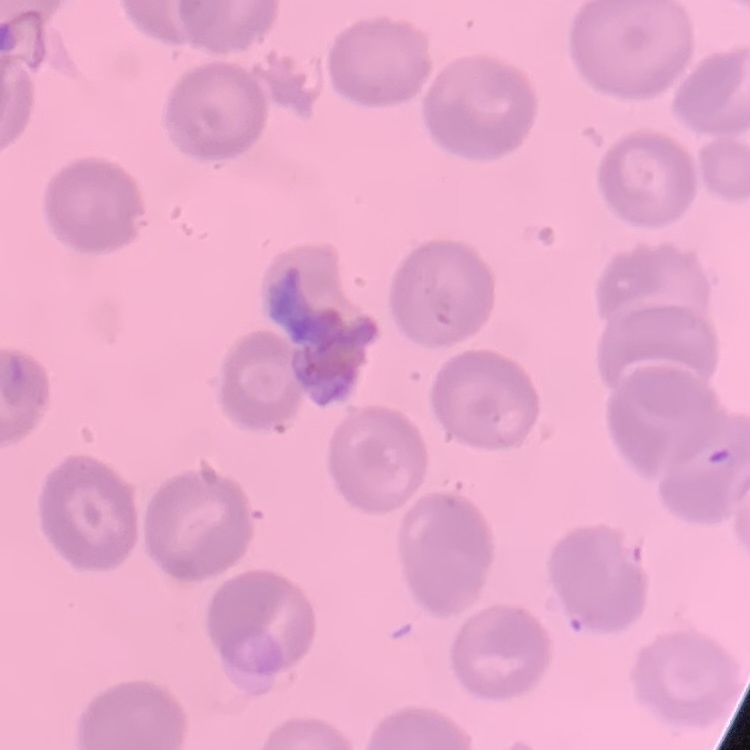
Summary:
  - Erythrocyte morphology: no rouleaux formation
  - Image type: square crop of a larger photomicrograph
  - Preparation: thin blood film
  - Stain: Field's or Giemsa